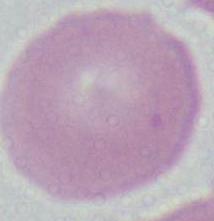
identification = red blood cell
magnification = 1000x
modality = micrograph